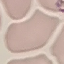
Malaria status: uninfected. Giemsa stain. Thin blood smear. Automatically extracted cell patch, resized to 64 × 64 pixels. Acquired by smartphone through the microscope eyepiece.